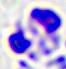

{
  "identification": "white blood cell",
  "magnification": "400x",
  "modality": "photomicrograph"
}